Outline each blood parasite and name the species.
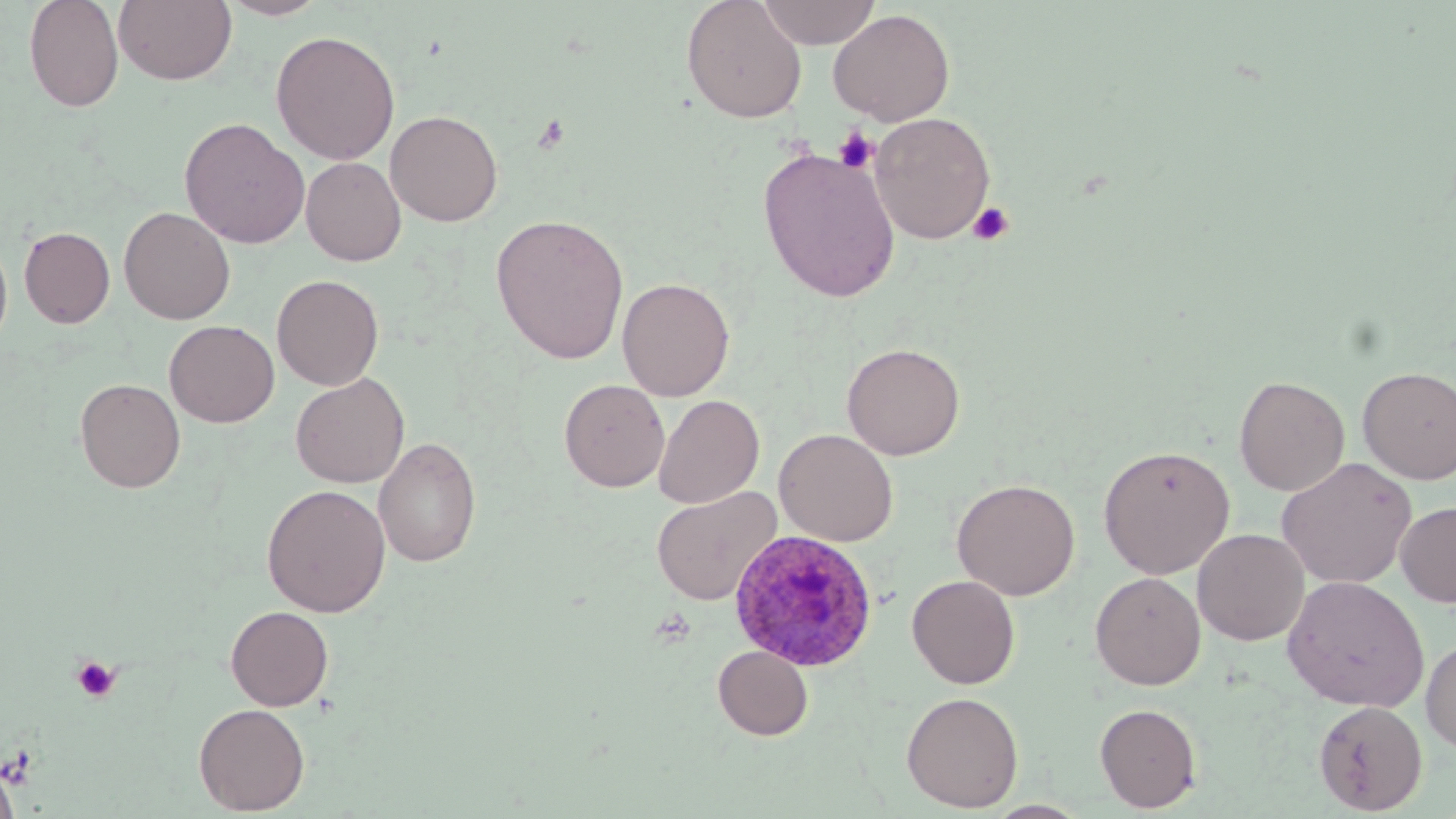
Approximate bounding boxes as (x1,y1)-(x2,y2) corner pairs in pixels.
Plasmodium ovale-infected red blood cells: (729,530)-(878,672).
No Plasmodium falciparum, Plasmodium malariae, Plasmodium vivax, Babesia divergens, or Trypanosoma brucei observed.

slide-level diagnosis = Plasmodium ovale
platelet locations = approximate bounding boxes as (x1,y1)-(x2,y2) corner pairs in pixels: (532,114)-(571,154), (833,126)-(879,174), (966,201)-(1014,246), (70,655)-(122,703)
stain = May-Grünwald-Giemsa
field of view = single
magnification = 1000x
uninfected red blood cell locations = approximate bounding boxes as (x1,y1)-(x2,y2) corner pairs in pixels: (23,0)-(124,112), (113,0)-(237,85), (217,0)-(331,20), (681,0)-(807,123), (756,0)-(880,48), (828,9)-(955,126), (270,30)-(400,165), (385,109)-(503,226), (870,113)-(996,243), (179,117)-(310,249), (757,146)-(901,302), (301,156)-(405,266), (119,206)-(235,324), (490,213)-(630,364), (18,226)-(115,328), (0,235)-(13,355), (272,274)-(384,390), (617,277)-(735,401), (164,320)-(279,427), (841,342)-(966,460), (1357,366)-(1456,484), (290,372)-(409,488), (1234,375)-(1350,496), (75,377)-(186,492), (559,379)-(669,492), (653,395)-(764,508), (774,428)-(897,546), (373,435)-(482,567), (1098,444)-(1236,579), (1276,457)-(1417,589), (952,478)-(1080,600), (261,484)-(391,617), (651,486)-(782,605), (1395,501)-(1456,607), (1192,528)-(1309,646), (1090,571)-(1206,690), (906,574)-(1020,689), (1282,575)-(1430,711), (225,605)-(333,711), (1421,635)-(1456,754), (712,645)-(813,740), (900,691)-(1024,812), (1313,699)-(1427,815), (193,703)-(310,815), (1094,703)-(1202,812), (0,760)-(20,819)
modality = optical microscopy
image size = 1456×819 pixels
preparation = thin blood film